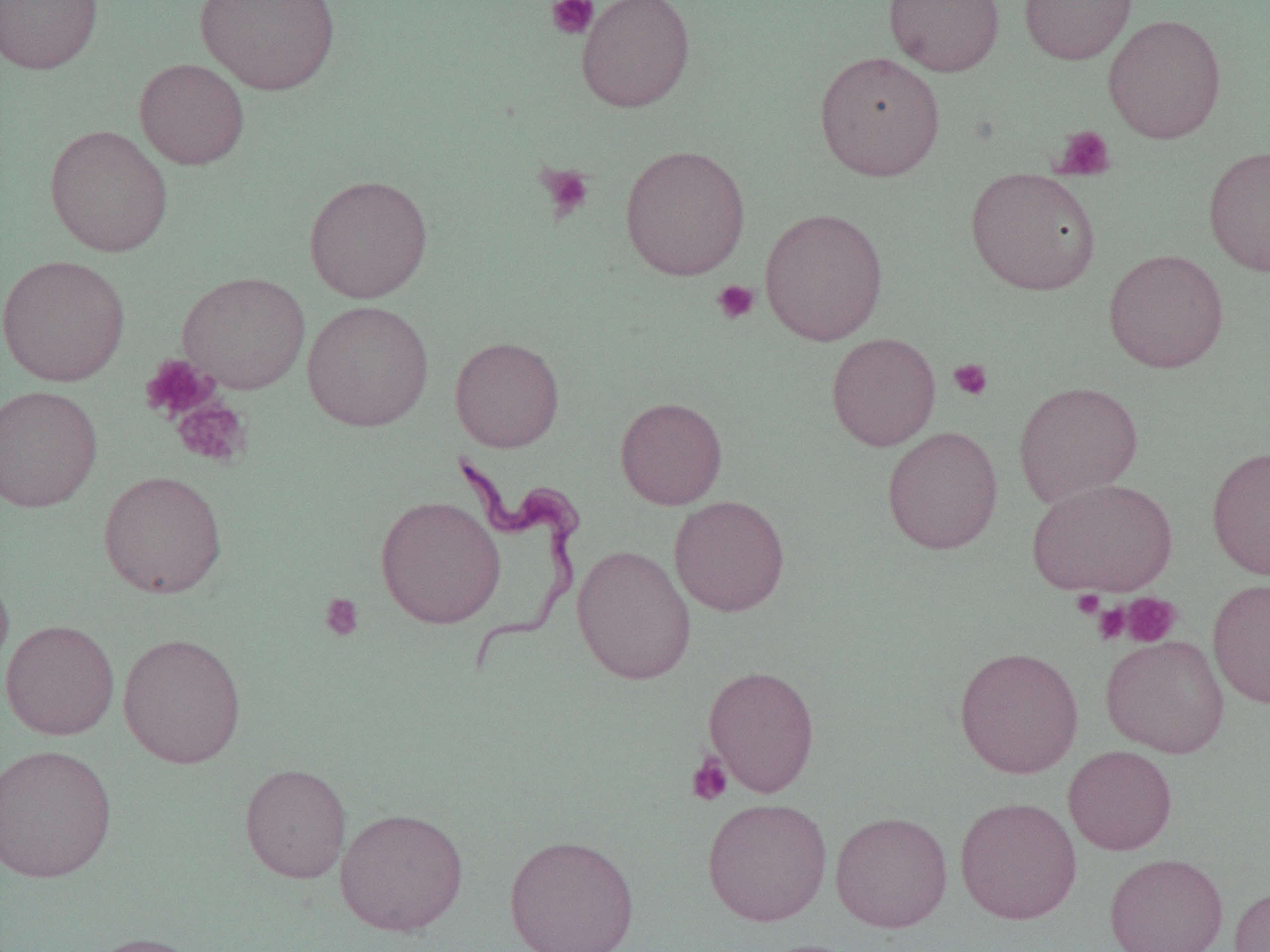

slide-level diagnosis = Trypanosoma brucei
field of view = single
uninfected red blood cell locations = approximate bounding boxes as (x1,y1)-(x2,y2) corner pairs in pixels: (0,0)-(103,75), (194,0)-(341,94), (576,0)-(695,112), (883,0)-(1004,76), (1018,0)-(1137,64), (1104,14)-(1226,144), (814,50)-(946,181), (135,58)-(249,169), (44,124)-(174,257), (619,144)-(751,280), (1204,144)-(1270,277), (965,168)-(1101,295), (303,174)-(434,303), (759,207)-(888,345), (1103,248)-(1229,373), (0,254)-(131,387), (177,271)-(310,394), (302,300)-(435,432), (826,332)-(941,451), (449,336)-(564,452), (1014,381)-(1143,507), (0,385)-(102,512), (615,396)-(727,510), (881,425)-(1003,555), (1207,445)-(1270,580), (98,470)-(227,599), (1027,477)-(1177,597), (375,495)-(506,629), (669,495)-(790,616), (572,544)-(697,685), (0,567)-(14,681), (1208,577)-(1270,709), (0,619)-(120,740), (117,632)-(247,768), (1100,635)-(1229,758), (954,646)-(1084,779), (703,664)-(820,797), (0,743)-(118,883), (1063,746)-(1177,855), (240,762)-(352,883), (954,796)-(1082,925), (702,797)-(832,926), (335,807)-(469,937), (830,810)-(953,932), (504,834)-(639,952), (1104,852)-(1228,952), (1229,885)-(1270,952), (82,932)-(205,952), (755,938)-(864,952)
platelet locations = approximate bounding boxes as (x1,y1)-(x2,y2) corner pairs in pixels: (545,0)-(599,40), (1053,125)-(1116,181), (536,163)-(594,221), (712,280)-(760,325), (140,354)-(220,423), (948,358)-(993,400), (171,397)-(252,469), (1072,590)-(1105,618), (318,592)-(365,642), (1120,592)-(1182,647), (1094,602)-(1130,645), (687,753)-(733,806)
Trypanosoma brucei locations = approximate bounding boxes as (x1,y1)-(x2,y2) corner pairs in pixels: (452,446)-(587,679)
modality = optical microscopy
image size = 1270×952 pixels
preparation = thin blood film
magnification = 1000x